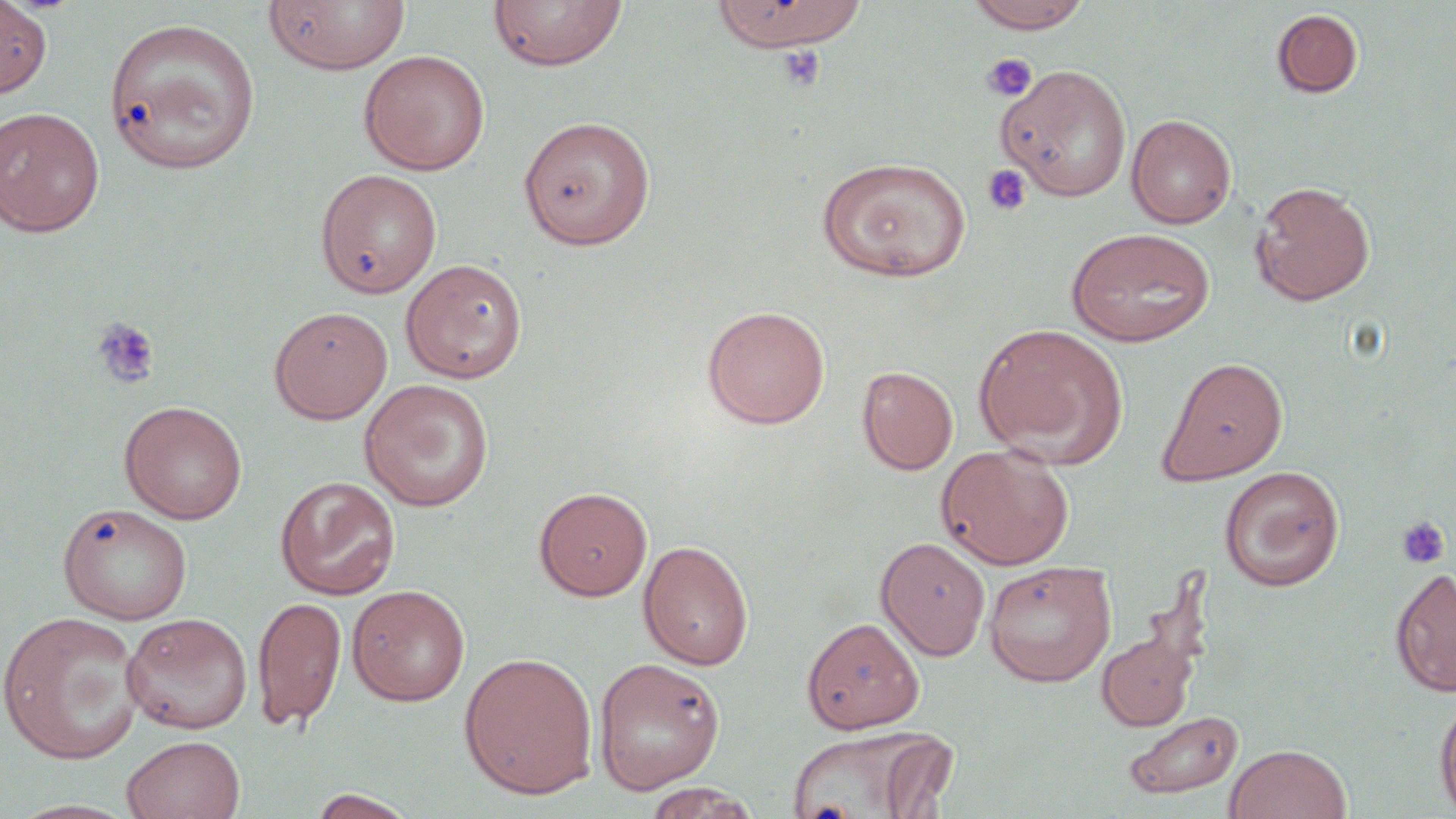 Approximate bounding boxes as (x1,y1)-(x2,y2) corner pairs in pixels. Platelet locations: (774,45)-(828,93), (982,54)-(1037,101), (981,164)-(1031,217), (91,316)-(161,389), (1396,515)-(1451,570). Uninfected red blood cell locations: (263,0)-(411,75), (711,0)-(867,53), (964,0)-(1093,33), (0,1)-(51,96), (488,1)-(628,72), (1271,8)-(1363,98), (103,16)-(262,175), (358,50)-(490,175), (998,64)-(1132,201), (0,106)-(105,237), (1126,113)-(1237,229), (518,115)-(655,249), (816,156)-(972,283), (315,169)-(442,297), (1249,181)-(1375,306), (1064,227)-(1217,347), (400,258)-(528,383), (268,305)-(392,424), (701,305)-(830,429), (974,323)-(1128,467), (1157,355)-(1289,485), (857,365)-(958,475), (359,379)-(495,511), (119,400)-(247,524), (935,444)-(1075,570), (1218,465)-(1344,591), (275,476)-(400,600), (534,486)-(652,600), (57,502)-(193,625), (875,536)-(991,660), (638,540)-(754,671), (876,546)-(1118,667), (983,560)-(1116,686), (1390,566)-(1456,697), (347,585)-(471,706), (253,595)-(347,730), (1,611)-(146,765), (121,612)-(253,735), (801,616)-(925,733), (1097,631)-(1199,731), (458,651)-(599,799), (591,656)-(725,794), (1435,694)-(1456,818), (1124,710)-(1243,800), (785,725)-(949,819), (877,733)-(961,817), (121,735)-(246,819), (1225,743)-(1352,819), (642,783)-(761,819), (307,789)-(419,818), (4,798)-(144,819). Slide-level diagnosis: negative for blood parasites. 1000x magnification. Light microscopy. Image is 1456×819 pixels. One field of a larger specimen. Thin blood film. May-Grünwald-Giemsa stain.